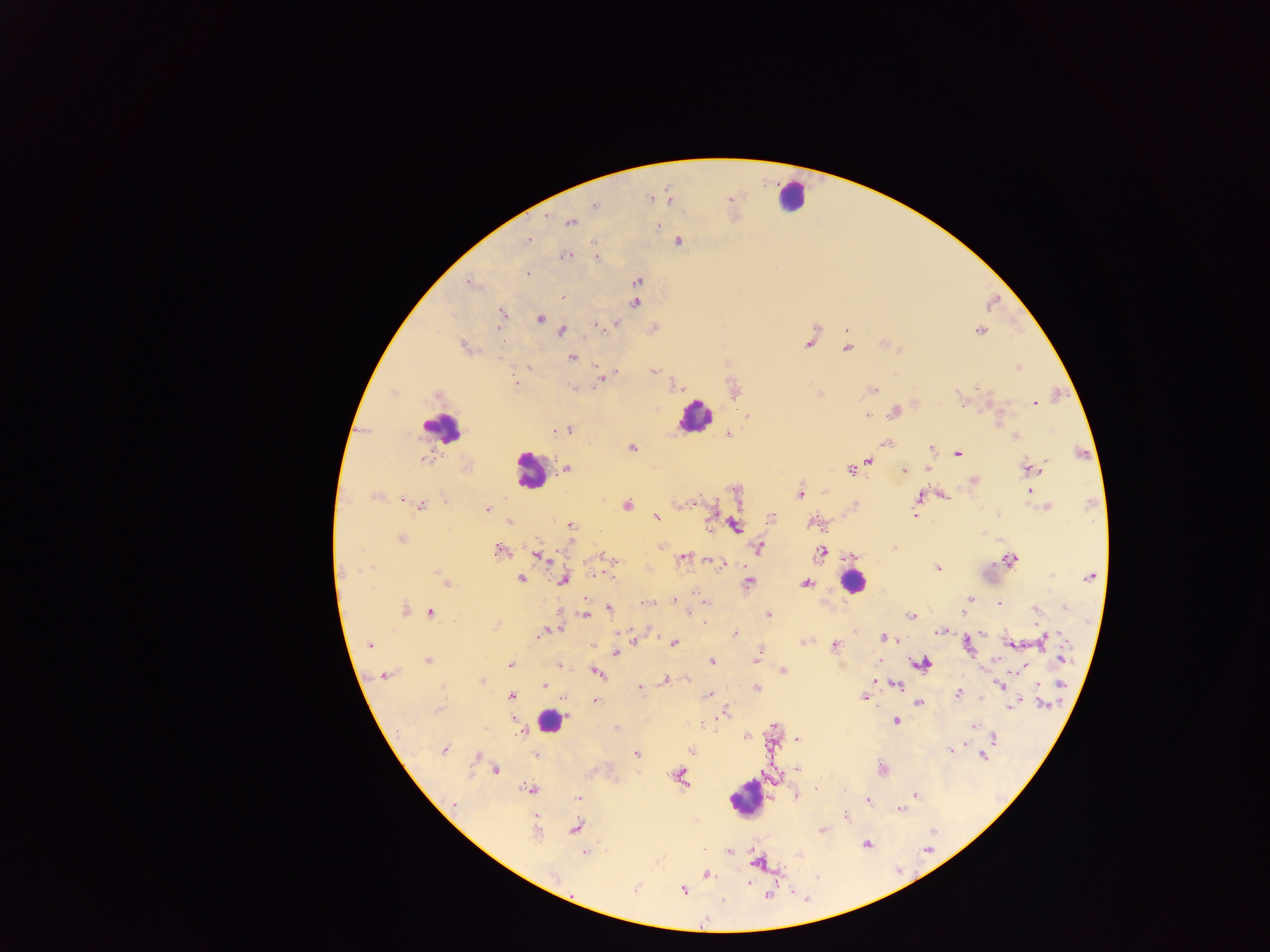

{
  "preparation": "thick blood smear",
  "capture": "mobile-phone photograph through a microscope",
  "field_of_view": "single",
  "leukocyte_locations": "approximate centers as [x, y] in pixels: [791, 196], [694, 416], [442, 427], [530, 470], [852, 582], [549, 720], [746, 799]",
  "image_size": "1270×952 pixels",
  "plasmodium_parasite_locations": "approximate centers as [x, y] in pixels: [669, 198], [650, 199], [595, 206], [570, 222], [658, 226], [528, 240], [679, 241], [595, 242], [566, 255], [596, 257], [528, 275], [637, 282], [470, 284], [563, 296], [635, 304], [502, 314], [540, 319], [616, 324], [597, 327], [498, 328], [562, 331], [980, 331], [808, 344], [464, 348], [846, 349], [573, 357], [1018, 367], [597, 368], [616, 371], [653, 372], [604, 375], [600, 380], [516, 384], [575, 387], [872, 390], [959, 398], [1034, 404], [895, 412], [867, 415], [568, 430], [555, 431], [728, 434], [1015, 437], [886, 443], [932, 447], [631, 448], [958, 453], [424, 459], [869, 461], [861, 465], [1030, 467], [567, 468], [928, 469], [904, 470], [851, 471], [973, 481], [1029, 491], [800, 494], [944, 496], [375, 497], [919, 497], [694, 503], [627, 505], [420, 506], [1046, 507], [486, 509], [915, 515], [657, 517], [772, 517], [510, 523], [571, 525], [734, 526], [400, 539], [661, 546], [759, 547], [892, 547], [499, 549], [822, 553], [538, 556], [683, 557], [614, 560], [1010, 560], [721, 565], [938, 569], [343, 572], [438, 572], [596, 574], [1091, 576], [520, 579], [563, 580], [446, 583], [749, 583], [806, 584], [970, 598], [674, 601], [703, 601], [647, 603], [999, 604], [965, 607], [1064, 607], [405, 609], [608, 609], [1036, 610], [962, 612], [431, 613], [688, 614], [586, 616], [768, 616], [911, 616], [496, 625], [939, 631], [547, 632], [982, 633], [735, 634], [541, 635], [884, 637], [634, 640], [1042, 640], [804, 641], [674, 643], [370, 644], [1010, 644], [835, 646], [968, 646], [615, 653], [757, 658], [1063, 658], [428, 661], [711, 661], [878, 661], [921, 663], [510, 664], [559, 665], [1023, 667], [782, 670], [596, 672], [385, 675], [687, 680], [875, 680], [666, 681], [481, 682], [897, 684], [544, 685], [1000, 685], [1061, 685], [640, 688], [757, 688], [957, 693], [709, 695], [511, 696], [863, 698], [982, 698], [595, 701], [919, 702], [1042, 704], [1012, 706], [438, 710], [726, 714], [513, 718], [896, 721], [973, 726], [523, 732], [747, 737], [994, 738], [797, 739], [444, 750], [691, 750], [950, 750], [637, 754], [536, 755], [477, 756], [982, 756], [799, 769], [495, 770], [882, 770], [680, 776], [530, 790], [796, 796], [916, 796], [578, 799], [867, 801], [455, 804], [899, 809], [846, 815], [576, 828], [822, 830], [536, 831], [866, 844], [729, 852], [584, 853], [756, 863], [554, 875], [706, 875], [749, 883], [635, 889], [683, 891], [767, 895], [705, 920]",
  "country": "Ghana"
}